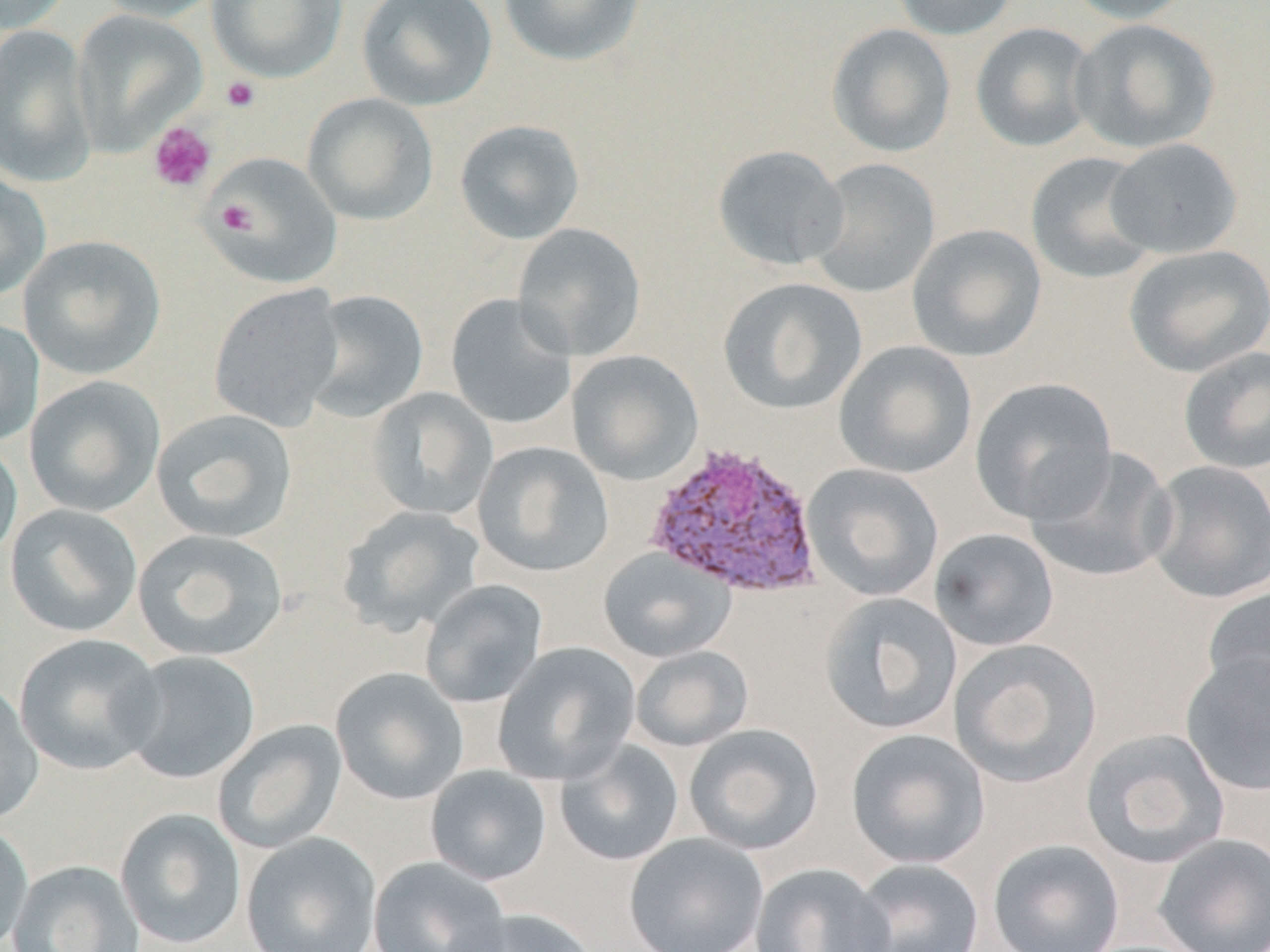
{
  "slide_level_diagnosis": "Plasmodium vivax",
  "magnification": "1000x",
  "plasmodium_vivax_infected_red_blood_cell_locations": "approximate bounding boxes as named x1/y1/x2/y2 corners in pixels: (x1=644, y1=440, x2=824, y2=599)",
  "modality": "light microscopy",
  "field_of_view": "single",
  "image_size": "1270×952 pixels",
  "uninfected_red_blood_cell_locations": "approximate bounding boxes as named x1/y1/x2/y2 corners in pixels: (x1=0, y1=0, x2=75, y2=34), (x1=90, y1=0, x2=227, y2=22), (x1=207, y1=0, x2=346, y2=83), (x1=356, y1=0, x2=498, y2=111), (x1=497, y1=0, x2=646, y2=67), (x1=891, y1=0, x2=1021, y2=40), (x1=1062, y1=0, x2=1196, y2=24), (x1=71, y1=9, x2=208, y2=156), (x1=1069, y1=18, x2=1220, y2=154), (x1=970, y1=22, x2=1098, y2=153), (x1=826, y1=23, x2=956, y2=158), (x1=0, y1=24, x2=97, y2=188), (x1=302, y1=93, x2=439, y2=225), (x1=454, y1=119, x2=585, y2=244), (x1=1104, y1=137, x2=1243, y2=260), (x1=711, y1=144, x2=850, y2=271), (x1=205, y1=151, x2=342, y2=289), (x1=1025, y1=151, x2=1161, y2=284), (x1=806, y1=158, x2=940, y2=299), (x1=0, y1=170, x2=51, y2=303), (x1=512, y1=223, x2=646, y2=361), (x1=907, y1=224, x2=1047, y2=362), (x1=18, y1=234, x2=165, y2=380), (x1=1124, y1=244, x2=1270, y2=378), (x1=717, y1=276, x2=867, y2=415), (x1=208, y1=284, x2=345, y2=432), (x1=303, y1=289, x2=429, y2=423), (x1=445, y1=293, x2=578, y2=430), (x1=0, y1=316, x2=44, y2=448), (x1=833, y1=340, x2=977, y2=479), (x1=1178, y1=346, x2=1270, y2=475), (x1=567, y1=350, x2=704, y2=485), (x1=24, y1=376, x2=165, y2=517), (x1=969, y1=377, x2=1118, y2=524), (x1=366, y1=388, x2=498, y2=521), (x1=152, y1=408, x2=298, y2=543), (x1=0, y1=435, x2=22, y2=565), (x1=473, y1=441, x2=614, y2=577), (x1=1024, y1=445, x2=1179, y2=584), (x1=1146, y1=459, x2=1269, y2=604), (x1=802, y1=463, x2=944, y2=602), (x1=4, y1=504, x2=142, y2=637), (x1=335, y1=505, x2=485, y2=637), (x1=929, y1=527, x2=1059, y2=652), (x1=133, y1=528, x2=289, y2=662), (x1=598, y1=548, x2=735, y2=663), (x1=419, y1=579, x2=548, y2=708), (x1=1202, y1=584, x2=1270, y2=715), (x1=818, y1=592, x2=963, y2=736), (x1=13, y1=633, x2=164, y2=776), (x1=949, y1=638, x2=1102, y2=788), (x1=492, y1=642, x2=641, y2=786), (x1=630, y1=645, x2=754, y2=752), (x1=118, y1=651, x2=261, y2=784), (x1=1180, y1=652, x2=1270, y2=796), (x1=330, y1=667, x2=469, y2=805), (x1=0, y1=681, x2=44, y2=826), (x1=212, y1=719, x2=347, y2=854), (x1=683, y1=723, x2=824, y2=855), (x1=1079, y1=727, x2=1230, y2=869), (x1=845, y1=728, x2=990, y2=869), (x1=554, y1=739, x2=685, y2=867), (x1=424, y1=765, x2=552, y2=886), (x1=114, y1=807, x2=246, y2=949), (x1=0, y1=820, x2=34, y2=951), (x1=240, y1=832, x2=382, y2=952), (x1=623, y1=832, x2=769, y2=952), (x1=1153, y1=834, x2=1270, y2=952), (x1=987, y1=838, x2=1125, y2=952), (x1=368, y1=856, x2=512, y2=952), (x1=850, y1=858, x2=985, y2=952), (x1=7, y1=859, x2=144, y2=952), (x1=749, y1=862, x2=893, y2=952), (x1=448, y1=907, x2=599, y2=952)",
  "preparation": "thin blood film",
  "platelet_locations": "approximate bounding boxes as named x1/y1/x2/y2 corners in pixels: (x1=220, y1=76, x2=260, y2=113), (x1=148, y1=121, x2=216, y2=193), (x1=216, y1=200, x2=256, y2=236)",
  "stain": "May-Grünwald-Giemsa"
}